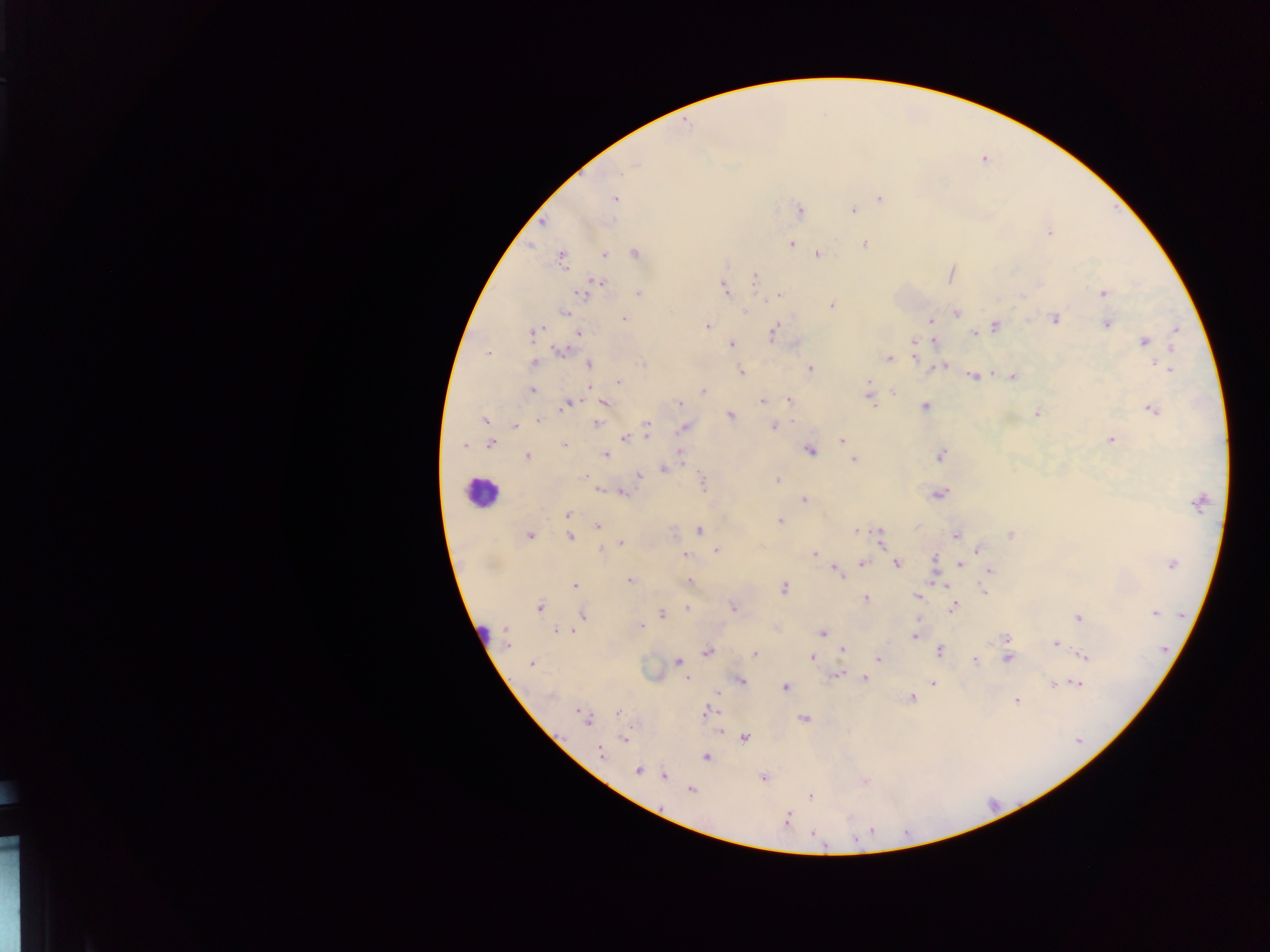
Approximate centers as {x, y} in pixels. Leukocyte locations: {485, 488}, {481, 627}. Plasmodium parasite locations: {615, 198}, {879, 198}, {797, 209}, {852, 211}, {1050, 234}, {791, 243}, {864, 244}, {635, 252}, {606, 254}, {817, 254}, {560, 260}, {600, 279}, {755, 279}, {724, 286}, {637, 293}, {1103, 293}, {581, 295}, {780, 295}, {832, 304}, {566, 311}, {956, 312}, {746, 313}, {1054, 319}, {624, 320}, {930, 321}, {1105, 324}, {993, 325}, {707, 327}, {538, 330}, {1177, 330}, {532, 332}, {773, 332}, {972, 332}, {578, 333}, {932, 340}, {1145, 341}, {913, 343}, {560, 351}, {488, 353}, {889, 358}, {918, 360}, {534, 362}, {590, 364}, {1158, 364}, {944, 366}, {934, 367}, {1167, 367}, {811, 368}, {739, 370}, {973, 376}, {1011, 376}, {870, 380}, {619, 381}, {532, 390}, {703, 390}, {893, 392}, {605, 401}, {788, 401}, {678, 402}, {762, 402}, {872, 403}, {572, 404}, {925, 407}, {562, 408}, {1151, 410}, {1036, 413}, {730, 415}, {485, 421}, {538, 421}, {595, 423}, {513, 424}, {772, 425}, {683, 428}, {646, 433}, {624, 439}, {1109, 439}, {842, 440}, {490, 443}, {565, 446}, {465, 447}, {810, 450}, {679, 451}, {607, 455}, {941, 455}, {528, 456}, {853, 458}, {664, 469}, {584, 474}, {638, 475}, {776, 480}, {703, 484}, {597, 488}, {624, 492}, {938, 495}, {802, 499}, {566, 515}, {781, 520}, {598, 528}, {701, 530}, {854, 531}, {530, 534}, {956, 534}, {1010, 534}, {569, 536}, {623, 542}, {882, 542}, {717, 549}, {601, 550}, {977, 550}, {814, 552}, {685, 555}, {935, 558}, {862, 561}, {896, 564}, {1170, 564}, {959, 566}, {989, 570}, {839, 575}, {688, 580}, {631, 581}, {575, 584}, {938, 584}, {784, 587}, {983, 591}, {865, 597}, {918, 597}, {953, 606}, {540, 607}, {686, 608}, {733, 608}, {661, 613}, {1153, 613}, {582, 614}, {1077, 618}, {641, 625}, {505, 630}, {556, 630}, {577, 630}, {821, 632}, {914, 637}, {1005, 639}, {508, 643}, {1055, 644}, {843, 649}, {939, 649}, {708, 652}, {754, 655}, {1084, 656}, {814, 657}, {877, 659}, {1007, 659}, {973, 661}, {531, 662}, {676, 662}, {863, 677}, {687, 678}, {742, 679}, {1078, 683}, {932, 684}, {1054, 684}, {785, 689}, {716, 694}, {912, 698}, {1017, 701}, {577, 711}, {705, 711}, {617, 713}, {802, 719}, {588, 722}, {719, 732}, {745, 737}, {623, 739}, {600, 753}, {706, 757}, {638, 772}, {664, 775}, {865, 782}, {690, 789}, {811, 797}, {787, 817}, {815, 836}. Image is 1270×952 pixels. Collected in Ghana. Thick blood smear. One field of view. Photographed through a microscope with a mobile-phone camera.